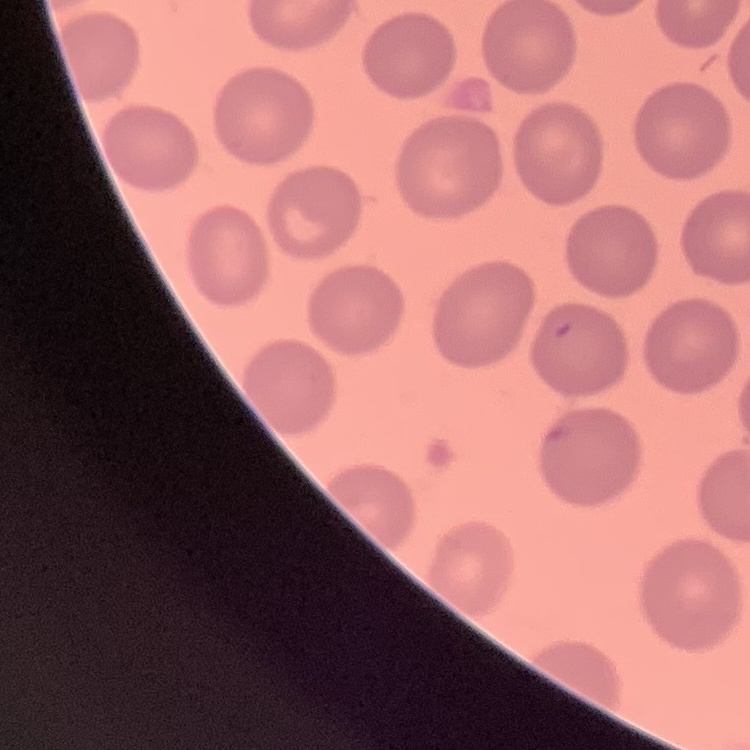

red blood cell morphology = no rouleaux formation
stain = Field's or Giemsa
image type = one tile cut from a larger photomicrograph
preparation = thin blood film